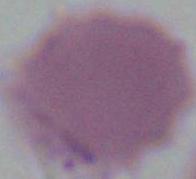
1000x magnification. A red blood cell is shown. Micrograph.